Point out each Plasmodium parasite.
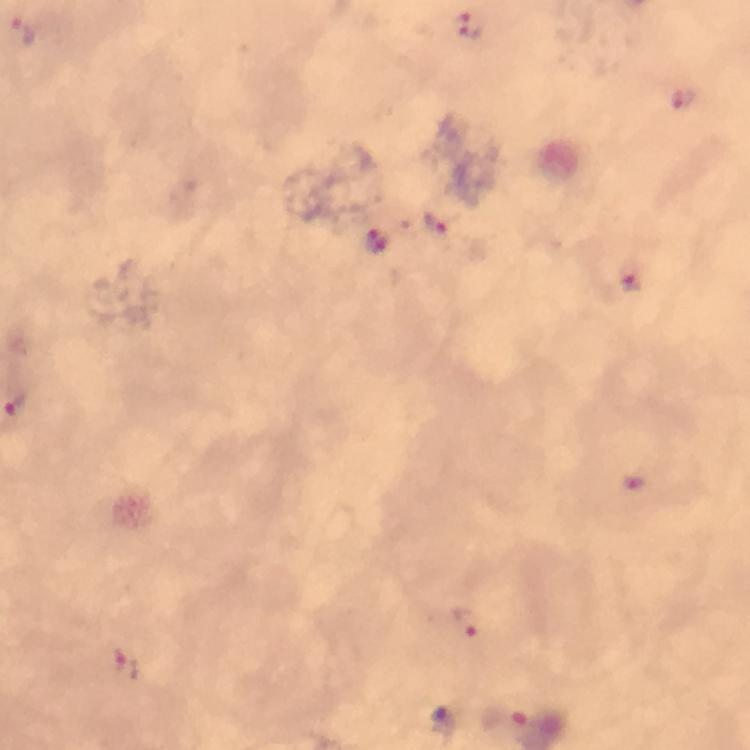
Approximate object centers, in pixels from the top-left corner.
Plasmodium parasites: (x=22, y=31), (x=473, y=33), (x=683, y=99), (x=440, y=222), (x=381, y=250), (x=635, y=280), (x=466, y=625), (x=504, y=720).

Smartphone photograph taken through a microscope. Image is 750×750 pixels. Immersion oil applied. At 100x magnification. From a malaria diagnostic workup. Thick blood smear. Giemsa stain. A crop from one field of view.